Classify this cell by malaria status.
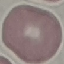

It is uninfected.

capture = smartphone camera at the microscope eyepiece
stain = Giemsa
image type = cell patch, automatically extracted from a larger field of view and resized to 64 × 64 pixels
preparation = thin smear